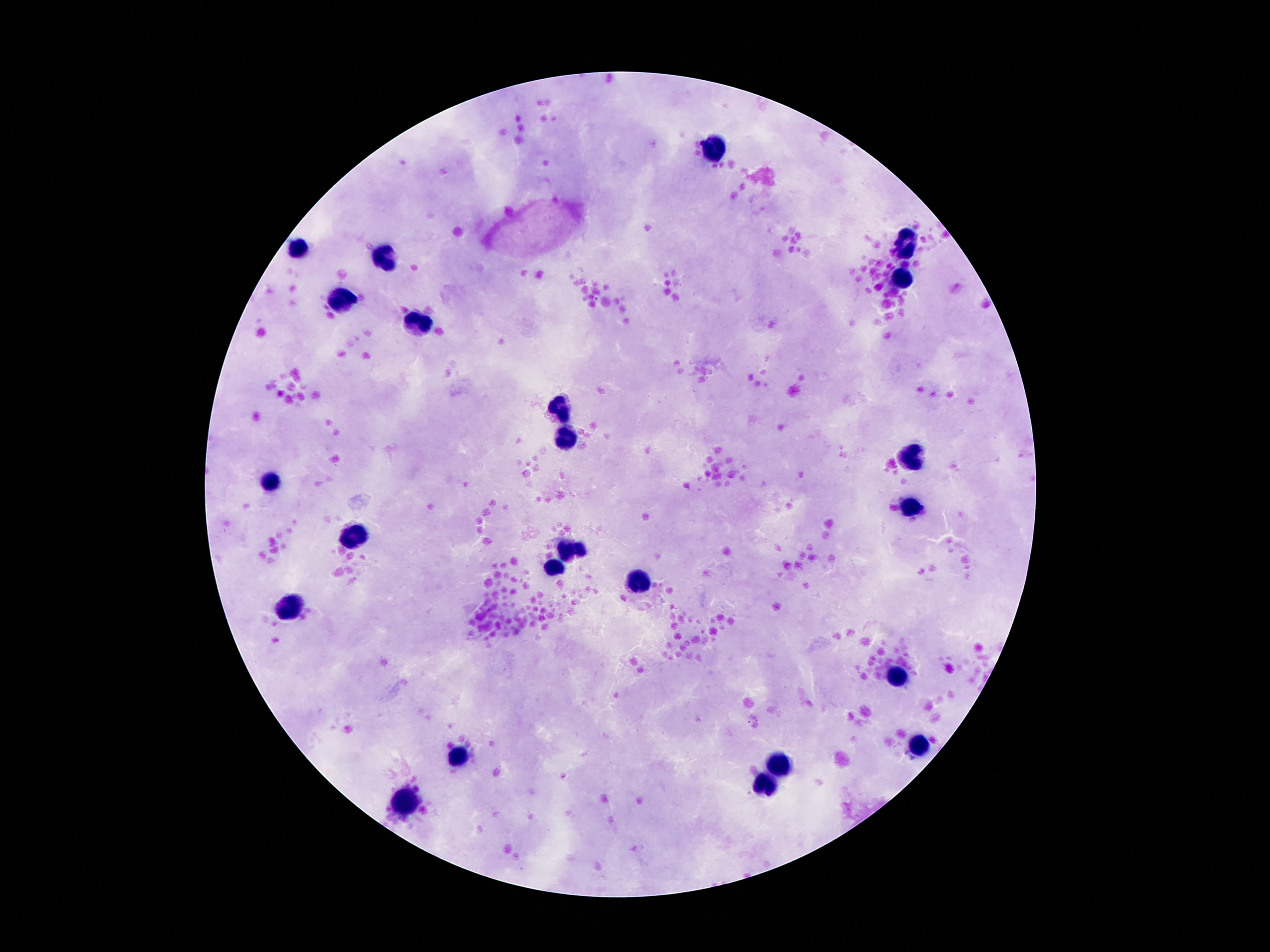

Approximate object centers, in pixels from the top-left corner.
Summary:
  - Leukocyte locations: (x=717, y=150), (x=295, y=247), (x=907, y=248), (x=386, y=257), (x=902, y=279), (x=343, y=301), (x=424, y=322), (x=561, y=408), (x=564, y=432), (x=914, y=455), (x=269, y=483), (x=912, y=506), (x=357, y=542), (x=563, y=550), (x=582, y=551), (x=554, y=565), (x=638, y=584), (x=289, y=607), (x=900, y=673), (x=924, y=742), (x=460, y=757), (x=778, y=764), (x=765, y=784), (x=405, y=805)
  - Capture: smartphone camera through the microscope eyepiece
  - Preparation: thick peripheral-blood smear
  - Stain: Giemsa
  - Field of view: single
  - Patient malaria status: uninfected
  - Image size: 1270×952 pixels
  - Magnification: 100x